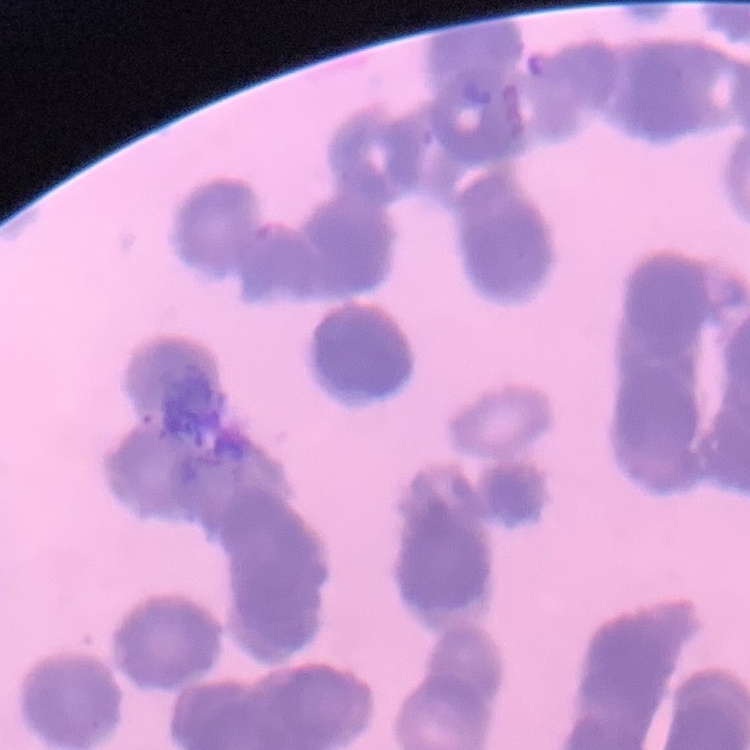

{
  "erythrocyte_morphology": "rouleaux formation",
  "image_type": "square crop of a larger photomicrograph",
  "stain": "Field's or Giemsa",
  "preparation": "thin blood smear"
}